Locate every uninfected red blood cell.
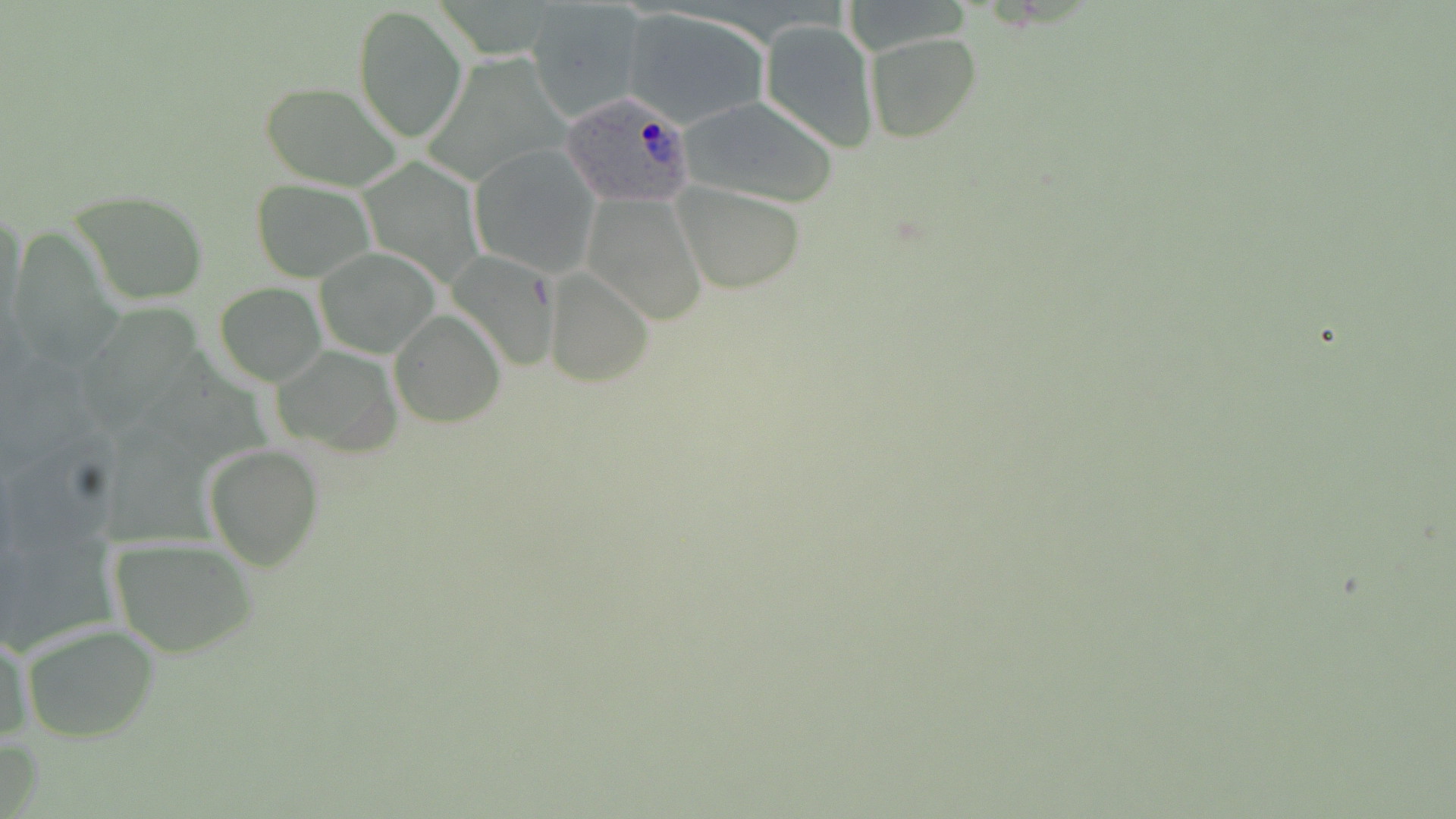
Approximate bounding boxes as [x1, y1, x2, y2] in pixels.
Uninfected red blood cells: [526, 1, 650, 121], [354, 5, 467, 141], [620, 7, 773, 129], [759, 17, 878, 152], [865, 31, 982, 143], [261, 81, 404, 190], [673, 94, 839, 208], [469, 146, 599, 275], [250, 179, 373, 281], [675, 182, 805, 292], [69, 190, 210, 306], [585, 194, 708, 326], [1, 206, 27, 340], [315, 246, 440, 358], [447, 252, 561, 373], [544, 268, 653, 386], [215, 283, 326, 385], [389, 310, 505, 427], [270, 345, 403, 457], [204, 444, 322, 569], [109, 537, 260, 659], [22, 623, 159, 743], [1, 628, 30, 746].

Summary:
  - Plasmodium ovale-infected red blood cell locations: [560, 90, 696, 206]
  - Slide-level diagnosis: Plasmodium ovale
  - Stain: May-Grünwald-Giemsa
  - Modality: optical microscopy
  - Field of view: one of a larger specimen
  - Image size: 1456×819 pixels
  - Magnification: 1000x
  - Preparation: thin blood film